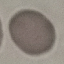

Result: no malaria parasites detected. Giemsa stain. Thin smear of blood. Photographed with a smartphone camera at the microscope eyepiece. Cell patch, automatically extracted from a larger field of view and resized to 64 × 64 pixels.